Classify this cell by malaria status.
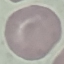

It is uninfected.

Thin blood film. Acquired by smartphone through the microscope eyepiece. Giemsa-stained preparation. Cell patch, automatically extracted from a larger field of view and resized to 64 × 64 pixels.